Give the extent of all Plasmodium malariae-infected red blood cells.
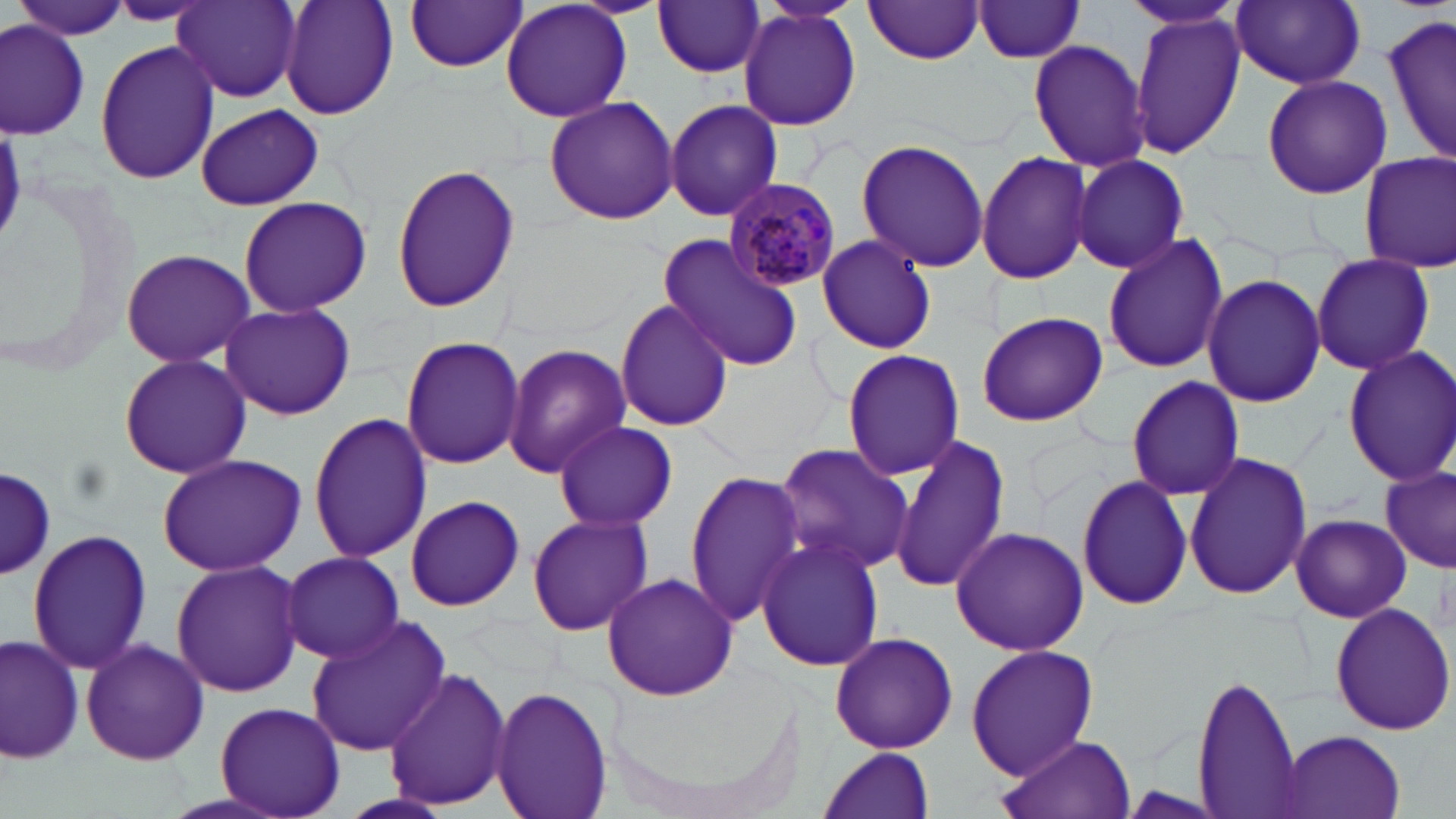
Approximate bounding boxes as (x1,y1)-(x2,y2) corner pairs in pixels.
Plasmodium malariae-infected red blood cells: (721,178)-(845,293).

Uninfected red blood cell locations: (280,0)-(400,119), (500,0)-(633,124), (1115,0)-(1249,32), (8,1)-(133,40), (404,1)-(529,73), (654,1)-(767,78), (862,1)-(987,63), (1230,1)-(1366,88), (104,2)-(211,26), (172,2)-(301,103), (968,2)-(1090,63), (738,8)-(863,132), (1130,10)-(1245,162), (1381,13)-(1456,167), (0,19)-(90,136), (1027,39)-(1150,172), (94,41)-(220,184), (1262,75)-(1391,199), (543,96)-(680,226), (663,98)-(783,221), (193,105)-(326,211), (854,138)-(990,272), (1357,150)-(1456,273), (977,151)-(1092,285), (1071,154)-(1190,275), (391,163)-(519,313), (237,195)-(371,317), (814,234)-(938,355), (1100,234)-(1227,373), (656,236)-(806,371), (119,247)-(259,367), (1310,255)-(1435,377), (1201,273)-(1325,408), (613,298)-(736,433), (217,303)-(357,421), (977,312)-(1107,427), (401,334)-(523,469), (503,343)-(630,473), (1342,346)-(1456,486), (841,349)-(964,481), (118,353)-(254,481), (1125,375)-(1246,502), (308,410)-(434,563), (553,420)-(677,529), (887,433)-(1012,594), (771,444)-(916,575), (1183,450)-(1310,601), (155,453)-(306,575), (1379,468)-(1455,573), (1,469)-(56,578), (684,471)-(808,626), (1077,475)-(1194,613), (404,496)-(525,611), (525,512)-(655,638), (1290,513)-(1410,623), (949,527)-(1090,656), (26,528)-(153,675), (755,534)-(884,673), (279,552)-(408,662), (171,558)-(306,697), (600,571)-(737,702), (1329,603)-(1455,735), (304,616)-(450,758), (829,629)-(957,756), (0,633)-(82,762), (81,637)-(210,766), (965,644)-(1099,778), (385,669)-(513,811), (1191,670)-(1303,819), (491,685)-(614,819), (214,701)-(347,817), (1279,730)-(1404,818), (997,732)-(1136,819), (817,747)-(936,819). Slide-level diagnosis: Plasmodium malariae. Image is 1456×819 pixels. Single field of view. May-Grünwald-Giemsa-stained preparation. Optical microscopy. Captured at 1000x magnification. Thin blood smear.